Report the malaria status of this cell.
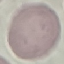
It is uninfected.

Acquired by smartphone through the microscope eyepiece. Giemsa stain. Automatically extracted cell patch, resized to 64 × 64 pixels. Thin blood smear.